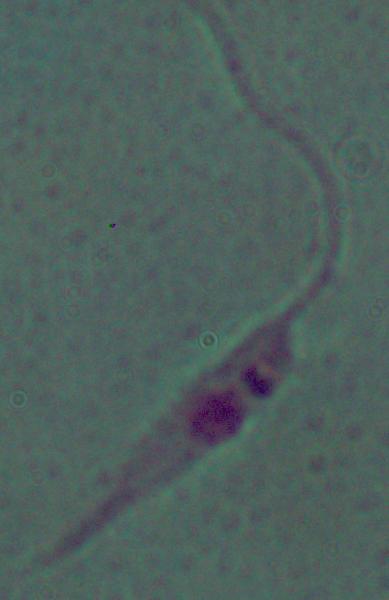
magnification: 1000x
modality: micrograph
identification: Leishmania